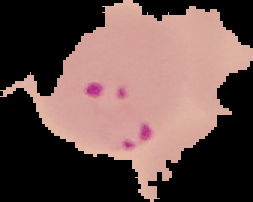
Summary:
  - Image size: 253×202 pixels
  - Preparation: thin blood smear
  - Image type: segmented cell region on a black background
  - Malaria status: parasitized